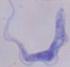

A trypanosome is shown. Captured at 1000x magnification. Micrograph.